Assess the morphology of the red blood cells.
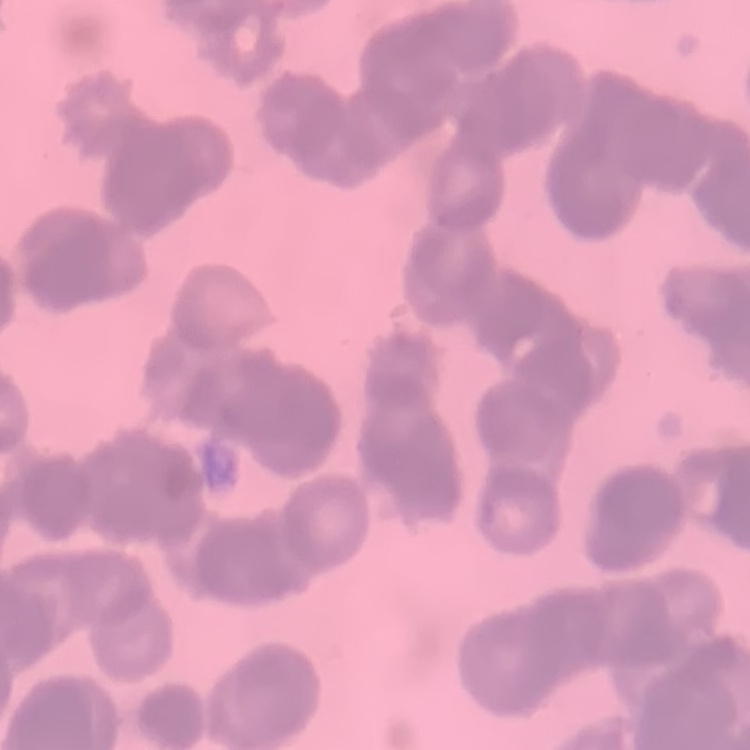
Rouleaux formation.

Summary:
  - Preparation: thin peripheral smear
  - Image type: one tile cut from a larger photomicrograph
  - Stain: Field's or Giemsa